Comment on the morphology of the red blood cells.
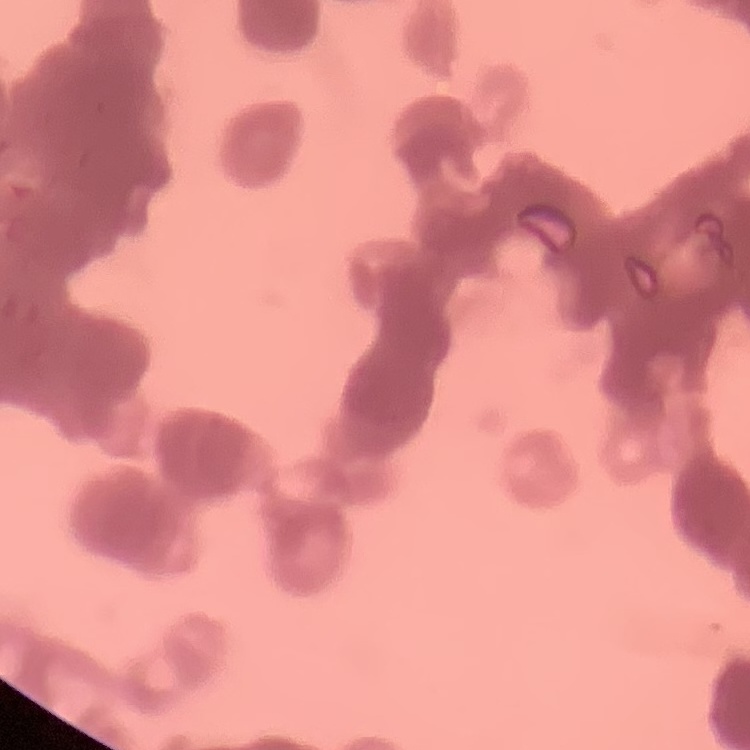
Rouleaux formation.

Square crop of a larger photomicrograph. Stained with either Field's or Giemsa. Thin blood film.